Point out each leukocyte.
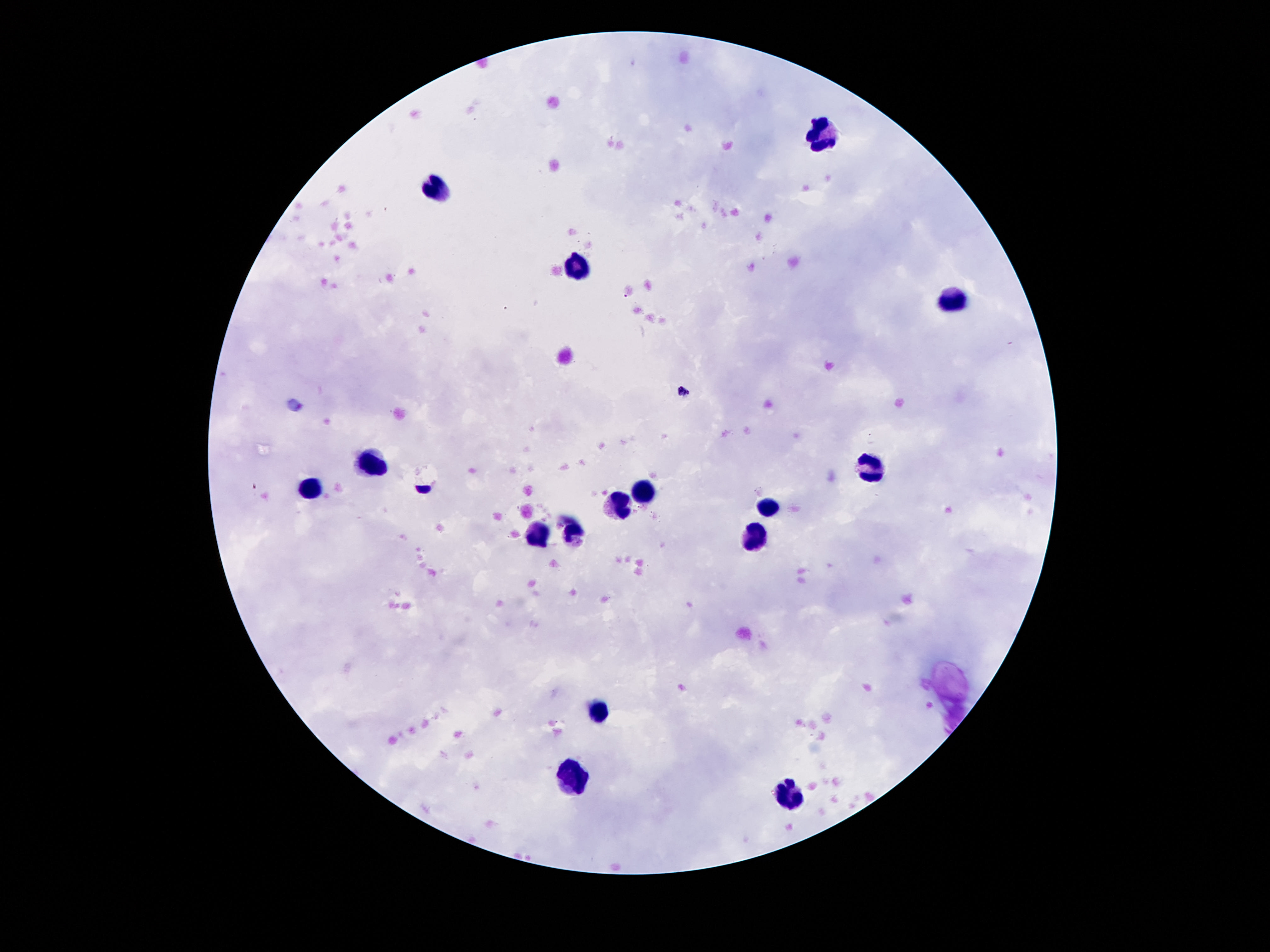
Approximate centers as (x, y) in pixels.
Leukocytes: (818, 135), (436, 189), (572, 267), (950, 300), (371, 463), (873, 465), (310, 490), (644, 492), (619, 503), (770, 509), (573, 532), (533, 538), (751, 539), (596, 709), (572, 778), (785, 794).

preparation = thick peripheral-blood smear
stain = Giemsa
capture = smartphone camera through the microscope eyepiece
field of view = single
image size = 1270×952 pixels
magnification = 100x
patient malaria status = uninfected